Describe the morphology of the erythrocytes.
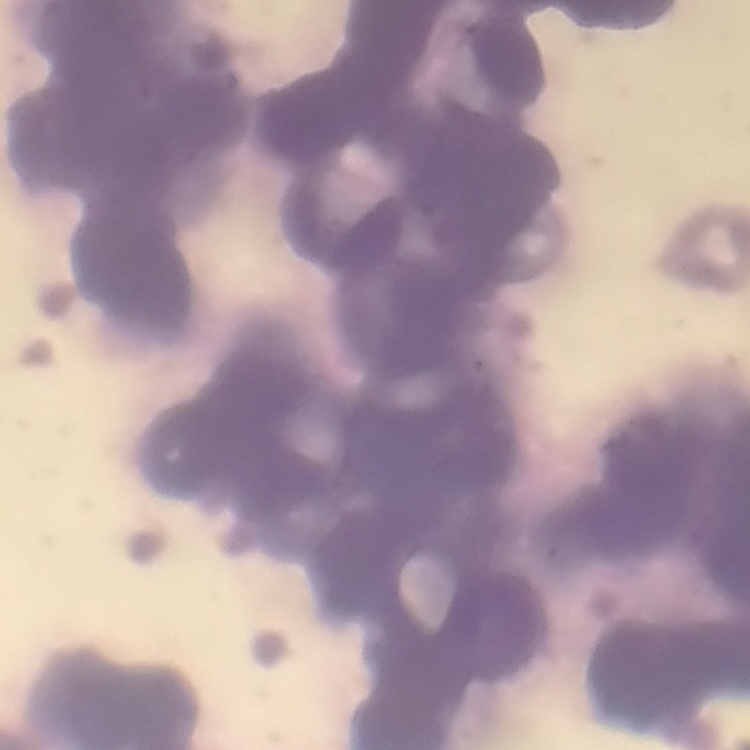
They show rouleaux formation.

Summary:
  - Preparation: thin peripheral smear
  - Stain: Field's or Giemsa
  - Image type: square crop of a larger photomicrograph